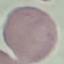
Result: no malaria parasites seen. Automatically extracted cell patch, resized to 64 × 64 pixels. Giemsa-stained preparation. Thin smear of blood. Photographed with a smartphone camera at the microscope eyepiece.